Report the malaria status of this cell.
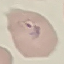

Parasitized.

image type = automatically extracted cell patch, resized to 64 × 64 pixels
preparation = thin blood smear
stain = Giemsa
capture = smartphone through the microscope eyepiece